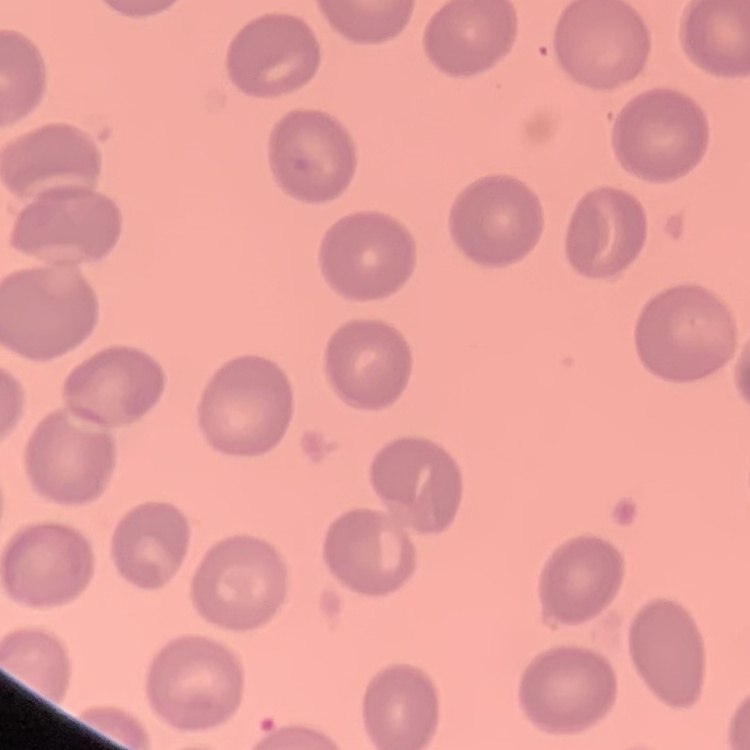
red blood cell morphology = no rouleaux formation
preparation = thin peripheral smear
image type = square crop of a larger photomicrograph
stain = Field's or Giemsa